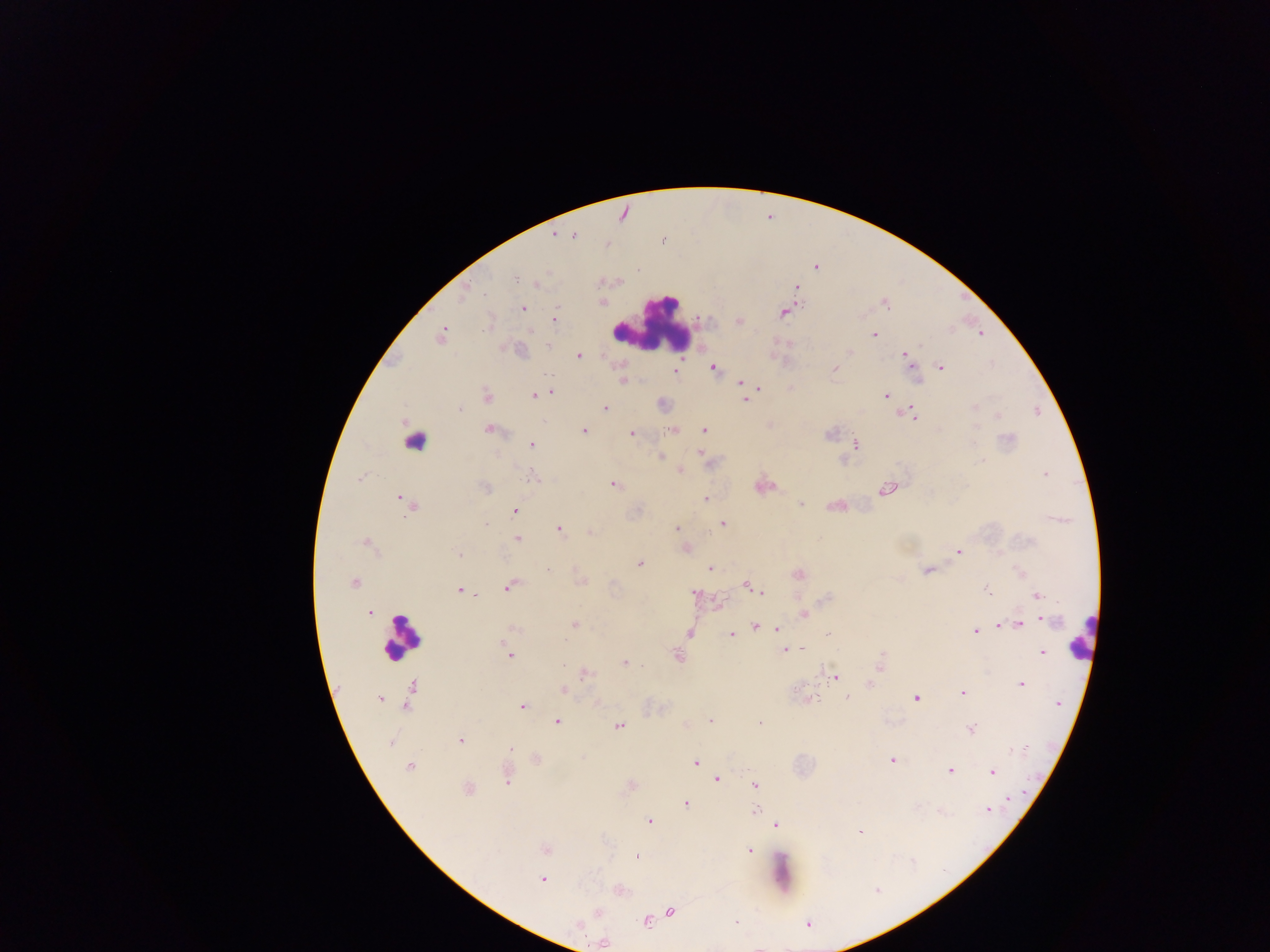 Approximate centers as (x, y) in pixels. Plasmodium parasite locations: (554, 235), (574, 236), (663, 240), (606, 244), (817, 268), (516, 277), (537, 283), (797, 287), (464, 294), (603, 302), (885, 304), (523, 308), (783, 312), (555, 319), (738, 321), (486, 324), (874, 335), (441, 336), (548, 346), (518, 351), (851, 352), (579, 356), (906, 357), (910, 363), (713, 367), (941, 367), (835, 368), (675, 371), (622, 381), (740, 383), (758, 387), (550, 392), (544, 394), (487, 396), (533, 396), (886, 396), (745, 400), (974, 407), (605, 408), (460, 409), (913, 415), (997, 415), (490, 429), (704, 429), (584, 430), (673, 430), (830, 433), (632, 434), (1008, 439), (975, 440), (531, 445), (855, 446), (699, 453), (660, 457), (981, 461), (680, 471), (1045, 475), (534, 478), (360, 479), (613, 485), (485, 487), (887, 489), (400, 498), (706, 499), (801, 504), (408, 506), (515, 511), (723, 523), (486, 525), (676, 528), (559, 529), (589, 532), (517, 539), (367, 543), (686, 548), (959, 552), (459, 554), (639, 563), (709, 569), (548, 570), (927, 570), (798, 575), (354, 582), (582, 582), (510, 586), (753, 588), (460, 590), (988, 590), (761, 592), (695, 594), (1037, 595), (475, 596), (369, 613), (804, 615), (1045, 620), (575, 624), (1020, 624), (1000, 626), (755, 627), (513, 628), (777, 628), (976, 631), (689, 634), (829, 634), (732, 635), (566, 641), (504, 645), (784, 650), (1042, 652), (510, 656), (677, 656), (563, 664), (625, 664), (880, 666), (586, 674), (835, 676), (870, 684), (1021, 684), (412, 688), (563, 689), (962, 692), (847, 697), (916, 698), (380, 699), (812, 700), (408, 702), (1058, 704), (523, 707), (710, 720), (557, 722), (759, 723), (618, 726), (971, 729), (460, 740), (390, 743), (511, 748), (537, 759), (891, 760), (695, 763), (409, 766), (950, 770), (992, 772), (507, 777), (718, 779), (755, 784), (468, 789), (1008, 799), (686, 803), (988, 809), (756, 810), (650, 821), (777, 825), (859, 832), (545, 850), (748, 850), (637, 857), (542, 879), (876, 890), (671, 911), (599, 912), (646, 921), (736, 923), (808, 924), (603, 943). Leukocyte locations: (651, 325), (419, 442), (401, 636), (1081, 637). One field of view. Mobile-phone photograph taken through the microscope. Image is 1270×952 pixels. Thick blood film. Collected in Ghana.